Name the blood parasite species.
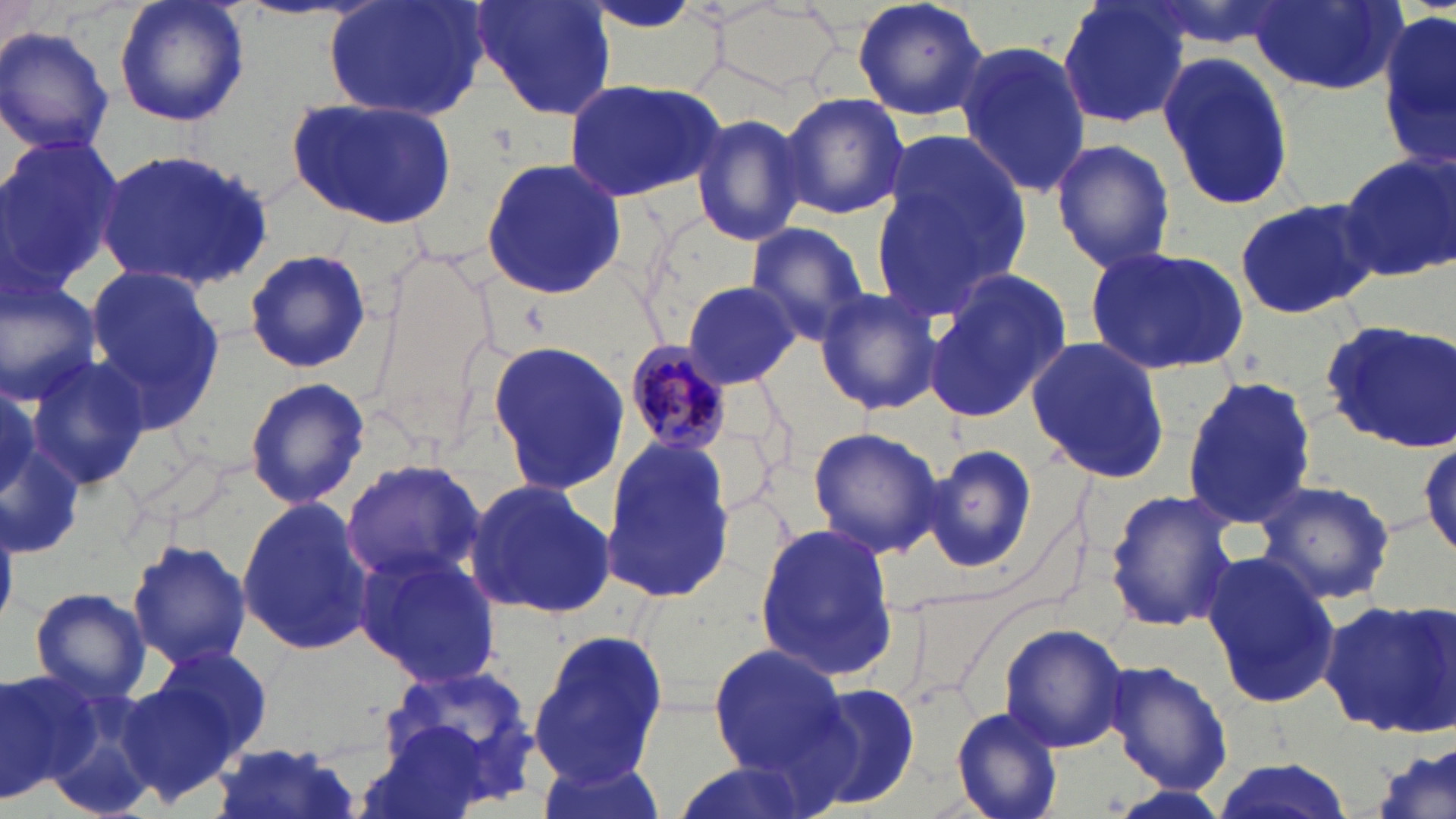

Plasmodium malariae.

Approximate bounding boxes as [x1, y1, x2, y2] in pixels. Plasmodium malariae-infected red blood cell locations: [622, 340, 733, 455]. Uninfected red blood cell locations: [112, 0, 250, 128], [324, 0, 490, 123], [468, 0, 618, 121], [849, 0, 991, 122], [1055, 0, 1193, 129], [1248, 1, 1405, 95], [0, 2, 47, 61], [704, 2, 847, 91], [1379, 9, 1456, 174], [0, 25, 115, 159], [955, 41, 1094, 199], [1160, 52, 1297, 211], [560, 77, 729, 207], [777, 92, 910, 219], [289, 95, 458, 229], [689, 112, 809, 248], [870, 126, 1032, 323], [0, 137, 122, 295], [1050, 137, 1177, 274], [96, 146, 272, 290], [1338, 151, 1456, 283], [479, 156, 627, 300], [1233, 197, 1377, 319], [744, 222, 873, 345], [1083, 244, 1249, 375], [242, 247, 372, 374], [78, 263, 225, 433], [921, 272, 1070, 425], [0, 274, 104, 403], [680, 280, 802, 389], [813, 287, 944, 416], [1320, 318, 1456, 453], [1025, 336, 1173, 485], [485, 339, 633, 496], [22, 357, 150, 487], [1179, 374, 1317, 531], [244, 377, 371, 509], [805, 425, 948, 557], [598, 433, 734, 603], [1413, 433, 1456, 558], [919, 442, 1040, 577], [340, 460, 484, 588], [463, 477, 615, 620], [1254, 479, 1397, 605], [1102, 487, 1242, 635], [235, 498, 375, 656], [753, 521, 898, 680], [125, 539, 253, 670], [352, 547, 503, 686], [1201, 549, 1343, 711], [29, 586, 152, 704], [1318, 597, 1456, 737], [997, 624, 1131, 755], [526, 628, 667, 787], [706, 643, 848, 775], [152, 646, 275, 762], [1104, 660, 1233, 795], [382, 661, 539, 796], [0, 666, 95, 801], [113, 673, 248, 806], [29, 681, 161, 818], [800, 682, 922, 812], [950, 706, 1067, 819], [1372, 740, 1455, 819], [206, 744, 367, 819], [540, 755, 665, 819], [1204, 756, 1355, 819], [665, 759, 817, 819]. Captured at 1000x magnification. One field of a larger specimen. Image is 1456×819 pixels. Optical microscopy. May-Grünwald-Giemsa stain. Thin blood smear.